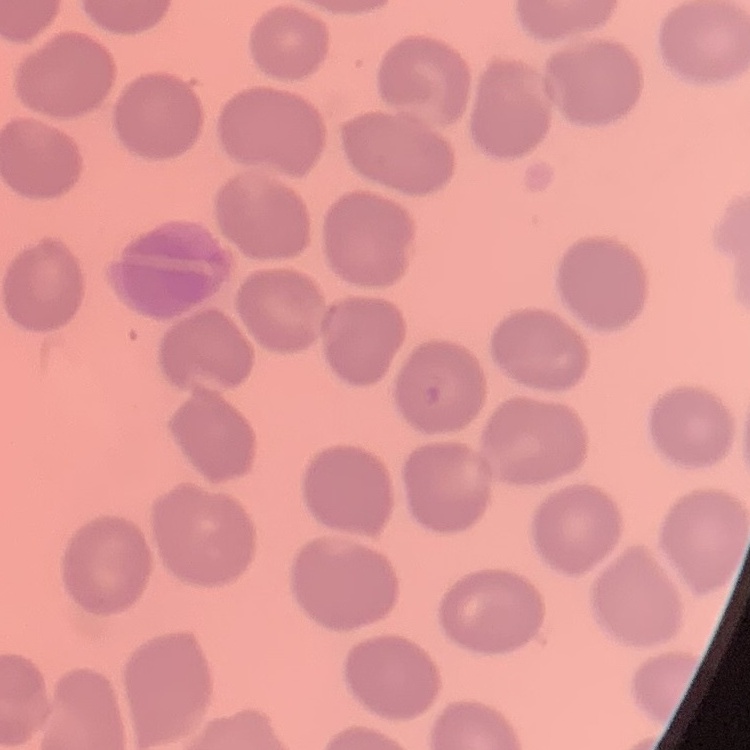
Summary:
  - Red blood cell morphology: no rouleaux formation
  - Image type: one tile cut from a larger photomicrograph
  - Preparation: thin blood film
  - Stain: Field's or Giemsa